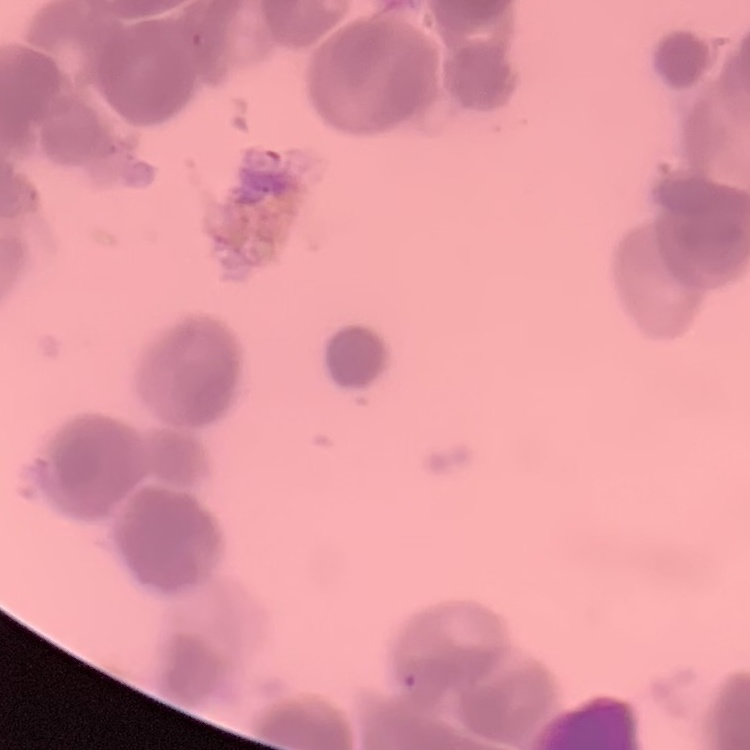
{
  "erythrocyte_morphology": "rouleaux formation",
  "image_type": "square crop of a larger photomicrograph",
  "preparation": "thin blood film",
  "stain": "Field's or Giemsa"
}